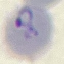
Summary:
  - Result: malaria parasites detected
  - Stain: Giemsa
  - Capture: smartphone through the microscope eyepiece
  - Preparation: thin blood smear
  - Image type: cell patch, automatically extracted from a larger field of view and resized to 64 × 64 pixels